Identify the cell.
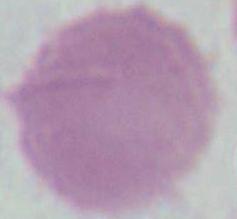
This is an erythrocyte.

Summary:
  - Magnification: 1000x
  - Modality: photomicrograph